Assess this cell for malaria.
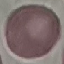
It is uninfected.

Summary:
  - Preparation: thin blood smear
  - Image type: cell patch, automatically extracted from a larger field of view and resized to 64 × 64 pixels
  - Stain: Giemsa
  - Capture: smartphone through the microscope eyepiece